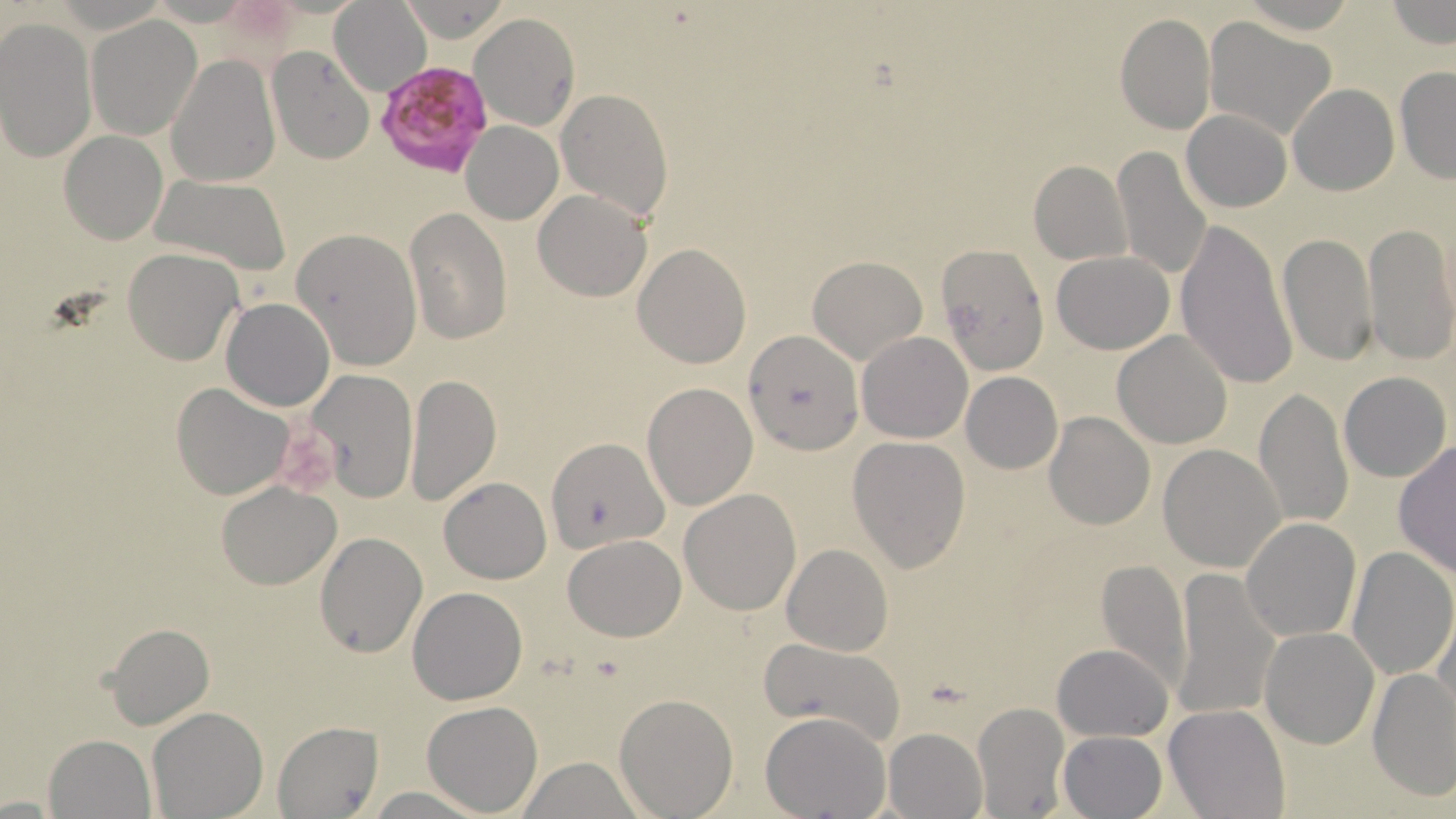

Summary:
  - Coordinate format: approximate bounding boxes as named x1/y1/x2/y2 corners in pixels
  - Plasmodium falciparum-infected red blood cell locations: (x1=373, y1=59, x2=496, y2=182)
  - Uninfected red blood cell locations: (x1=396, y1=0, x2=512, y2=42), (x1=1385, y1=0, x2=1454, y2=50), (x1=330, y1=2, x2=431, y2=95), (x1=1115, y1=12, x2=1216, y2=135), (x1=85, y1=13, x2=203, y2=141), (x1=469, y1=13, x2=579, y2=132), (x1=1203, y1=17, x2=1335, y2=141), (x1=0, y1=20, x2=96, y2=163), (x1=266, y1=45, x2=375, y2=164), (x1=166, y1=54, x2=280, y2=187), (x1=1394, y1=68, x2=1456, y2=182), (x1=1288, y1=85, x2=1398, y2=195), (x1=556, y1=87, x2=672, y2=223), (x1=1181, y1=109, x2=1291, y2=212), (x1=460, y1=122, x2=562, y2=224), (x1=60, y1=130, x2=168, y2=245), (x1=1111, y1=145, x2=1216, y2=282), (x1=1029, y1=161, x2=1131, y2=266), (x1=152, y1=175, x2=292, y2=274), (x1=532, y1=190, x2=652, y2=301), (x1=405, y1=207, x2=512, y2=345), (x1=1175, y1=217, x2=1297, y2=392), (x1=1363, y1=221, x2=1455, y2=364), (x1=290, y1=228, x2=422, y2=370), (x1=1278, y1=232, x2=1377, y2=366), (x1=631, y1=243, x2=752, y2=368), (x1=940, y1=243, x2=1046, y2=370), (x1=123, y1=247, x2=243, y2=365), (x1=1051, y1=250, x2=1174, y2=353), (x1=807, y1=254, x2=927, y2=365), (x1=222, y1=297, x2=335, y2=412), (x1=743, y1=329, x2=861, y2=454), (x1=1112, y1=330, x2=1233, y2=447), (x1=858, y1=331, x2=972, y2=443), (x1=304, y1=368, x2=419, y2=504), (x1=1339, y1=371, x2=1451, y2=482), (x1=961, y1=372, x2=1062, y2=475), (x1=406, y1=373, x2=501, y2=507), (x1=642, y1=382, x2=758, y2=511), (x1=171, y1=383, x2=293, y2=499), (x1=1253, y1=388, x2=1356, y2=528), (x1=1045, y1=411, x2=1154, y2=529), (x1=547, y1=434, x2=665, y2=554), (x1=846, y1=435, x2=972, y2=573), (x1=1392, y1=442, x2=1456, y2=580), (x1=1159, y1=444, x2=1285, y2=572), (x1=439, y1=477, x2=552, y2=584), (x1=216, y1=481, x2=340, y2=588), (x1=679, y1=488, x2=801, y2=614), (x1=1242, y1=517, x2=1360, y2=642), (x1=315, y1=532, x2=428, y2=659), (x1=563, y1=534, x2=686, y2=641), (x1=783, y1=544, x2=893, y2=656), (x1=1347, y1=546, x2=1456, y2=681), (x1=1093, y1=559, x2=1192, y2=695), (x1=1172, y1=571, x2=1279, y2=723), (x1=407, y1=586, x2=527, y2=704), (x1=1432, y1=603, x2=1456, y2=722), (x1=104, y1=623, x2=214, y2=730), (x1=1260, y1=628, x2=1378, y2=748), (x1=758, y1=635, x2=906, y2=748), (x1=1053, y1=644, x2=1173, y2=742), (x1=1366, y1=667, x2=1455, y2=802), (x1=614, y1=693, x2=739, y2=818), (x1=423, y1=701, x2=543, y2=816), (x1=972, y1=702, x2=1070, y2=817), (x1=1164, y1=705, x2=1290, y2=818), (x1=147, y1=706, x2=268, y2=819), (x1=760, y1=712, x2=891, y2=819), (x1=272, y1=721, x2=382, y2=817), (x1=882, y1=727, x2=986, y2=819), (x1=1058, y1=730, x2=1166, y2=817), (x1=43, y1=735, x2=157, y2=818), (x1=516, y1=756, x2=645, y2=819), (x1=362, y1=786, x2=490, y2=818)
  - Slide-level diagnosis: Plasmodium falciparum
  - Modality: light microscopy
  - Magnification: 1000x
  - Stain: May-Grünwald-Giemsa
  - Preparation: thin blood smear
  - Image size: 1456×819 pixels
  - Field of view: one of a larger specimen